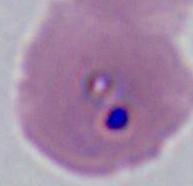

modality = photomicrograph
magnification = 400x or 1000x
identification = Plasmodium